Comment on the morphology of the erythrocytes.
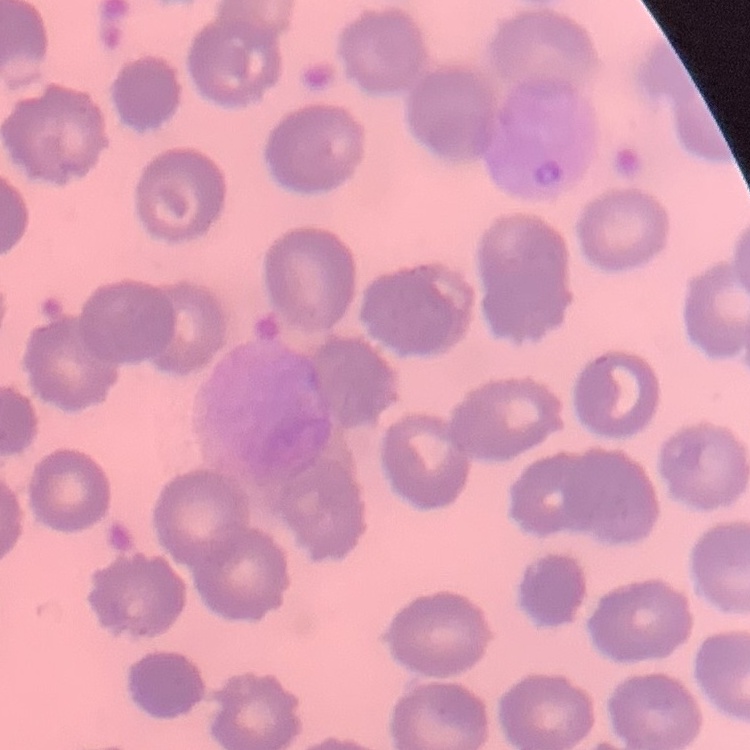

No rouleaux formation.

Summary:
  - Stain: Field's or Giemsa
  - Preparation: thin blood film
  - Image type: one tile cut from a larger photomicrograph